Classify this cell by malaria status.
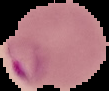

Parasitized.

preparation = thin blood smear
image size = 109×91 pixels
image type = segmented cell region on a black background